Classify this cell by malaria status.
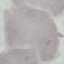
It is uninfected.

stain = Giemsa
image type = cell patch, automatically extracted from a larger field of view and resized to 64 × 64 pixels
preparation = thin blood smear
capture = smartphone through the microscope eyepiece